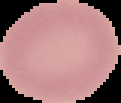

preparation = thin blood smear
image type = segmented cell region on a black background
image size = 121×103 pixels
result = negative for Plasmodium parasites